Report the malaria status of this cell.
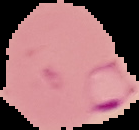
Parasitized.

image size = 139×130 pixels
image type = segmented cell region on a black background
preparation = thin blood film